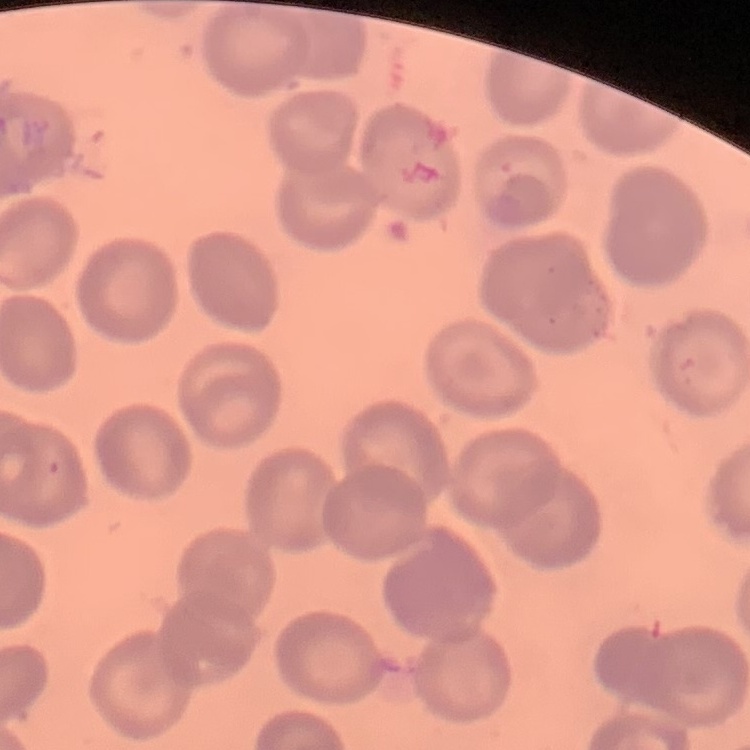
Summary:
  - Erythrocyte morphology: no rouleaux formation
  - Preparation: thin peripheral smear
  - Image type: square crop of a larger photomicrograph
  - Stain: Field's or Giemsa